Locate and identify every blood parasite.
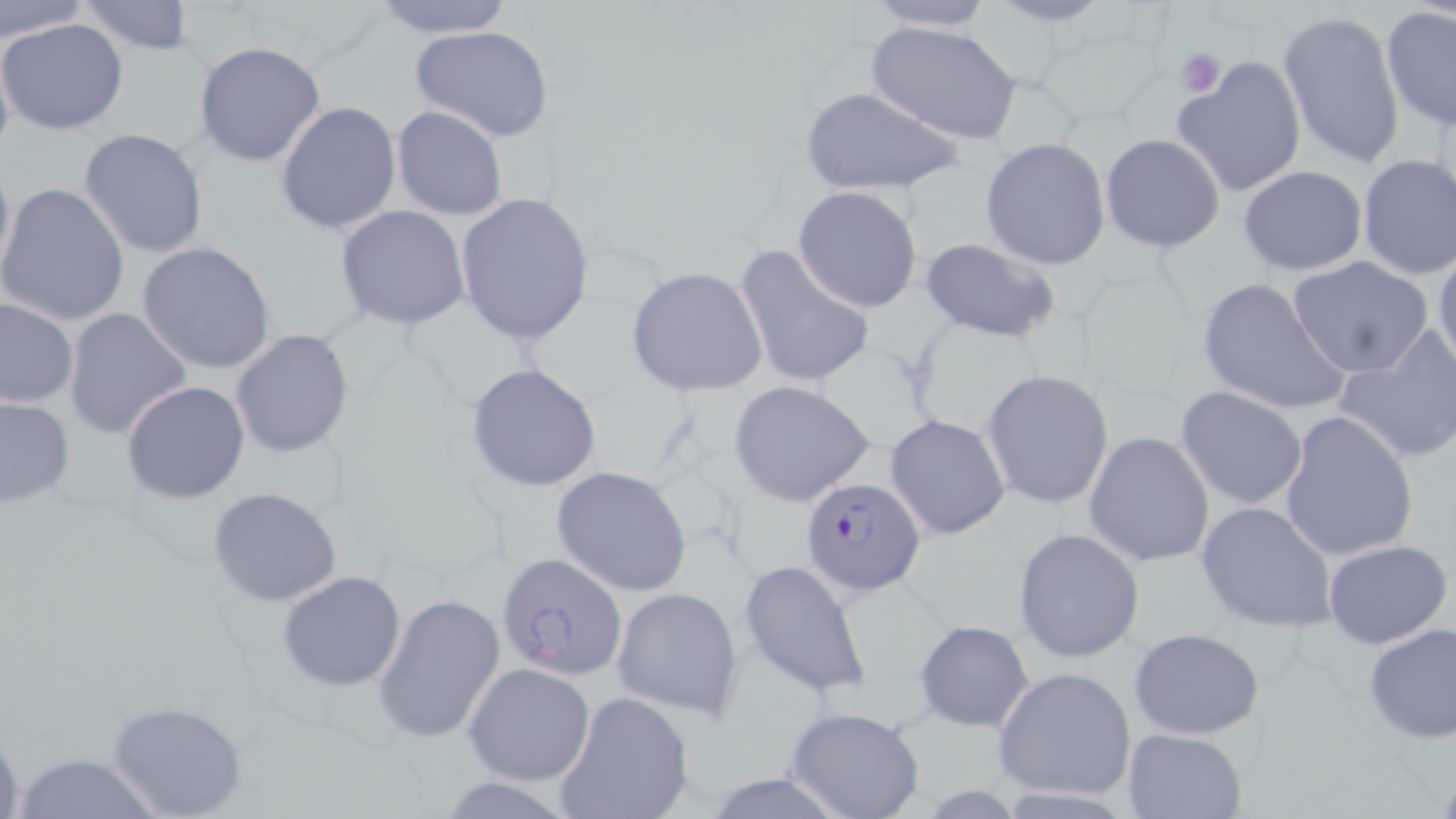

Approximate bounding boxes as (x1,y1)-(x2,y2) corner pairs in pixels.
Plasmodium falciparum-infected red blood cells: (800,477)-(927,599), (497,555)-(628,681).
No Plasmodium ovale, Plasmodium malariae, Plasmodium vivax, Babesia divergens, or Trypanosoma brucei observed.

slide-level diagnosis = Plasmodium falciparum
uninfected red blood cell locations = approximate bounding boxes as (x1,y1)-(x2,y2) corner pairs in pixels: (0,0)-(85,45), (364,0)-(518,39), (978,0)-(1121,29), (72,1)-(199,56), (860,1)-(999,32), (1380,6)-(1456,132), (1277,10)-(1405,172), (0,17)-(130,136), (866,21)-(1022,145), (406,25)-(556,143), (0,40)-(16,170), (192,42)-(325,168), (1174,56)-(1308,196), (800,87)-(965,196), (275,101)-(401,233), (390,105)-(509,221), (77,128)-(209,260), (1100,133)-(1226,254), (980,137)-(1111,270), (0,148)-(15,283), (1356,155)-(1456,281), (1239,165)-(1366,276), (0,183)-(131,326), (792,185)-(923,313), (453,192)-(596,348), (334,205)-(472,331), (918,237)-(1063,344), (137,242)-(276,375), (733,243)-(877,393), (1432,243)-(1456,373), (1288,257)-(1433,377), (626,265)-(769,397), (1196,275)-(1351,417), (0,298)-(78,408), (64,308)-(191,438), (1332,326)-(1456,464), (229,328)-(354,459), (464,363)-(602,492), (981,369)-(1115,509), (121,381)-(250,504), (727,381)-(876,507), (1176,386)-(1308,510), (0,396)-(75,510), (1189,396)-(1325,614), (1278,412)-(1418,562), (885,413)-(1012,541), (1083,431)-(1216,569), (550,465)-(695,597), (208,487)-(344,607), (1196,500)-(1337,633), (1013,527)-(1145,663), (1323,538)-(1452,650), (737,557)-(873,701), (277,570)-(406,692), (613,587)-(744,719), (372,592)-(506,744), (913,618)-(1036,732), (1361,621)-(1456,746), (1129,627)-(1266,740), (463,663)-(595,785), (993,666)-(1137,802), (552,691)-(697,819), (104,699)-(247,818), (784,706)-(925,819), (0,723)-(24,819), (1122,728)-(1245,818), (9,750)-(162,819)
modality = optical microscopy
preparation = thin blood film
image size = 1456×819 pixels
magnification = 1000x
stain = May-Grünwald-Giemsa
platelet locations = approximate bounding boxes as (x1,y1)-(x2,y2) corner pairs in pixels: (1175,47)-(1226,98)
field of view = single